Outline every leukocyte.
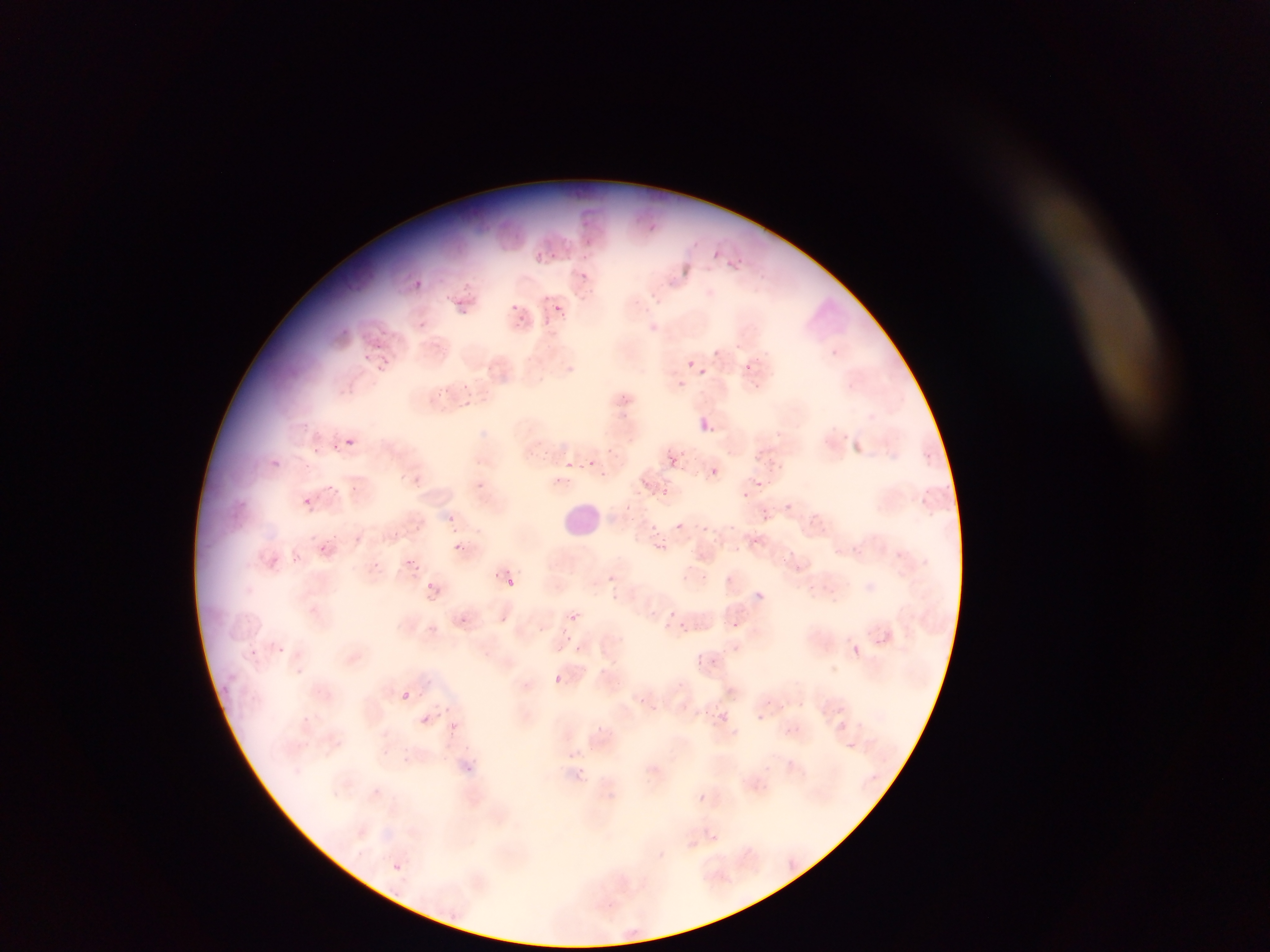
No leukocytes observed.

Approximate bounding boxes as left top right bottom in pixels.
Summary:
  - Plasmodium parasite locations: 647 224 658 235; 585 239 597 250; 529 249 552 265; 550 251 561 265; 709 251 720 258; 581 255 589 264; 738 256 750 263; 727 260 737 270; 577 269 587 283; 413 279 424 289; 354 281 366 291; 461 281 472 293; 539 292 551 303; 454 299 462 307; 508 301 526 311; 554 304 565 314; 458 307 478 318; 518 314 529 330; 543 315 553 327; 420 319 428 326; 379 326 389 337; 375 341 386 351; 361 350 369 357; 378 355 392 378; 686 360 696 369; 743 363 753 373; 695 366 708 376; 677 380 686 389; 460 382 475 400; 464 399 478 413; 698 418 713 433; 345 437 355 446; 331 442 341 456; 313 443 321 450; 271 456 278 465; 669 457 679 467; 586 459 596 468; 767 459 781 469; 566 460 574 470; 304 463 311 471; 710 469 720 477; 600 470 608 479; 412 474 420 485; 556 476 567 486; 758 480 769 488; 329 483 334 491; 351 485 360 493; 661 489 672 497; 741 492 749 499; 304 497 314 507; 562 500 606 536; 784 501 795 512; 622 503 630 510; 761 506 773 519; 449 515 458 522; 675 521 684 530; 702 523 715 531; 415 524 427 535; 650 524 659 531; 751 535 763 542; 655 539 670 550; 450 542 466 552; 319 543 330 551; 784 547 797 559; 895 551 901 559; 293 554 307 564; 405 558 418 565; 492 571 502 580; 607 573 617 583; 424 576 437 589; 506 577 514 586; 755 591 764 601; 609 595 620 602; 668 609 677 617; 570 613 579 623; 460 615 473 631; 499 618 508 622; 731 621 740 630; 679 623 689 634; 564 625 573 638; 874 639 883 647; 731 644 741 653; 277 646 286 652; 576 646 582 654; 852 646 861 655; 251 649 261 656; 698 652 717 669; 296 667 303 675; 553 675 562 684; 221 685 233 696; 404 688 414 699; 399 691 411 699; 637 695 646 703; 764 698 774 706; 707 708 716 716; 722 709 730 717; 420 714 430 725; 755 714 765 722; 449 722 457 729; 596 724 605 732; 847 741 861 752; 569 747 579 754; 467 765 478 773; 578 768 587 779; 697 793 707 803; 394 861 404 872 | approximate x y pixel centers of objects too small to bound: 447 294; 343 327; 543 627
  - Preparation: thin blood smear
  - Country: Ghana
  - Capture: mobile-phone photograph through a microscope
  - Field of view: single
  - Image size: 1270×952 pixels